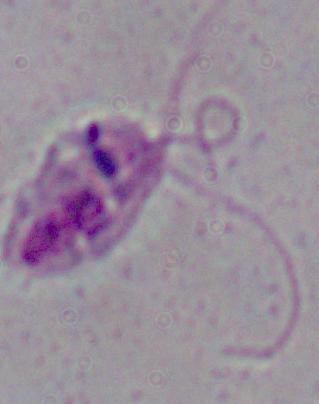
modality: micrograph
magnification: 1000x
identification: Leishmania